Outline each blood parasite and name the species.
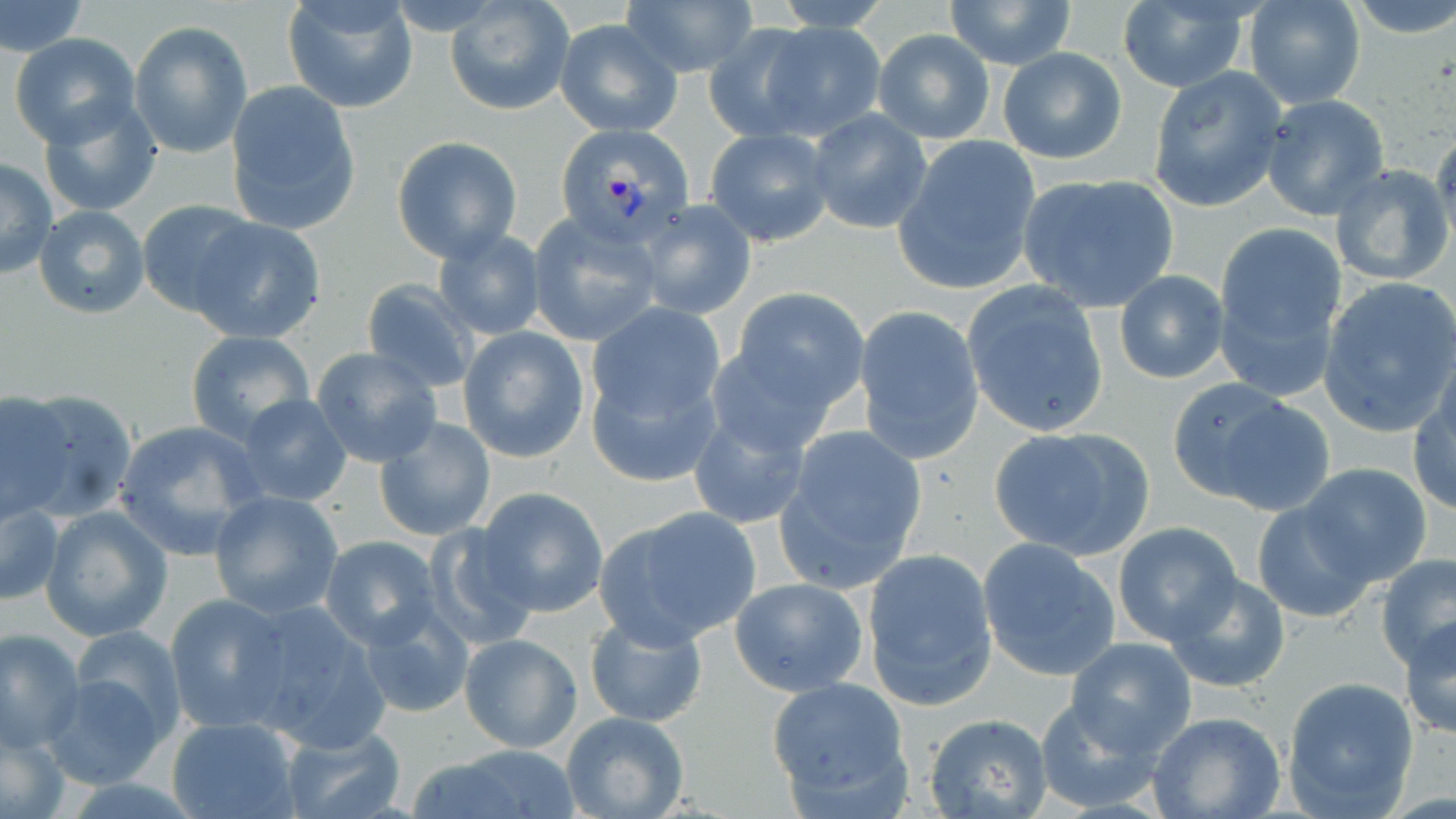

Approximate bounding boxes as named x1/y1/x2/y2 corners in pixels.
Plasmodium vivax-infected red blood cells: (x1=551, y1=127, x2=691, y2=252).
No Plasmodium falciparum, Plasmodium ovale, Plasmodium malariae, Babesia divergens, or Trypanosoma brucei observed.

Uninfected red blood cell locations: (x1=0, y1=0, x2=87, y2=58), (x1=282, y1=0, x2=417, y2=112), (x1=618, y1=0, x2=758, y2=79), (x1=765, y1=0, x2=900, y2=31), (x1=944, y1=0, x2=1076, y2=69), (x1=1243, y1=0, x2=1366, y2=110), (x1=1349, y1=0, x2=1456, y2=40), (x1=445, y1=1, x2=574, y2=115), (x1=1116, y1=1, x2=1252, y2=92), (x1=555, y1=18, x2=682, y2=135), (x1=129, y1=20, x2=252, y2=159), (x1=755, y1=20, x2=888, y2=140), (x1=703, y1=24, x2=823, y2=141), (x1=872, y1=30, x2=996, y2=145), (x1=10, y1=34, x2=141, y2=149), (x1=998, y1=46, x2=1127, y2=165), (x1=1147, y1=66, x2=1288, y2=213), (x1=225, y1=83, x2=360, y2=235), (x1=38, y1=92, x2=165, y2=220), (x1=1260, y1=93, x2=1390, y2=219), (x1=806, y1=109, x2=933, y2=236), (x1=705, y1=128, x2=834, y2=246), (x1=1430, y1=129, x2=1456, y2=252), (x1=392, y1=136, x2=523, y2=263), (x1=893, y1=136, x2=1042, y2=296), (x1=0, y1=159, x2=56, y2=279), (x1=1330, y1=163, x2=1456, y2=285), (x1=1017, y1=173, x2=1180, y2=312), (x1=136, y1=198, x2=260, y2=316), (x1=635, y1=200, x2=757, y2=320), (x1=33, y1=203, x2=150, y2=319), (x1=527, y1=216, x2=661, y2=346), (x1=189, y1=217, x2=327, y2=344), (x1=1213, y1=221, x2=1346, y2=378), (x1=433, y1=229, x2=546, y2=341), (x1=1112, y1=270, x2=1230, y2=384), (x1=1317, y1=276, x2=1456, y2=436), (x1=359, y1=279, x2=478, y2=392), (x1=962, y1=280, x2=1111, y2=438), (x1=730, y1=287, x2=871, y2=411), (x1=588, y1=302, x2=726, y2=429), (x1=854, y1=305, x2=985, y2=461), (x1=458, y1=327, x2=589, y2=462), (x1=185, y1=330, x2=314, y2=444), (x1=705, y1=333, x2=852, y2=454), (x1=310, y1=346, x2=443, y2=468), (x1=586, y1=363, x2=723, y2=490), (x1=1408, y1=375, x2=1456, y2=517), (x1=1166, y1=379, x2=1314, y2=511), (x1=0, y1=392, x2=76, y2=521), (x1=234, y1=394, x2=353, y2=508), (x1=686, y1=407, x2=813, y2=530), (x1=374, y1=416, x2=495, y2=541), (x1=113, y1=418, x2=266, y2=559), (x1=773, y1=424, x2=928, y2=592), (x1=988, y1=425, x2=1155, y2=561), (x1=1298, y1=464, x2=1433, y2=585), (x1=474, y1=487, x2=610, y2=617), (x1=209, y1=491, x2=344, y2=619), (x1=1, y1=498, x2=63, y2=607), (x1=1251, y1=499, x2=1381, y2=624), (x1=38, y1=506, x2=173, y2=642), (x1=596, y1=506, x2=762, y2=648), (x1=425, y1=521, x2=541, y2=647), (x1=1113, y1=523, x2=1242, y2=645), (x1=320, y1=537, x2=442, y2=648), (x1=976, y1=540, x2=1122, y2=682), (x1=862, y1=545, x2=998, y2=712), (x1=1376, y1=555, x2=1456, y2=666), (x1=1166, y1=574, x2=1291, y2=693), (x1=730, y1=577, x2=871, y2=698), (x1=164, y1=594, x2=297, y2=733), (x1=357, y1=600, x2=474, y2=719), (x1=239, y1=601, x2=391, y2=747), (x1=584, y1=610, x2=707, y2=727), (x1=1402, y1=616, x2=1456, y2=742), (x1=0, y1=627, x2=84, y2=753), (x1=67, y1=627, x2=188, y2=751), (x1=458, y1=633, x2=582, y2=752), (x1=1066, y1=636, x2=1197, y2=756), (x1=39, y1=671, x2=171, y2=792), (x1=766, y1=675, x2=913, y2=812), (x1=1281, y1=675, x2=1421, y2=818), (x1=1032, y1=695, x2=1166, y2=812), (x1=562, y1=711, x2=690, y2=819), (x1=1149, y1=712, x2=1286, y2=819), (x1=924, y1=714, x2=1054, y2=819), (x1=167, y1=717, x2=299, y2=819), (x1=1, y1=723, x2=69, y2=819), (x1=278, y1=726, x2=408, y2=819), (x1=412, y1=744, x2=583, y2=818). Slide-level diagnosis: Plasmodium vivax. Light microscopy. Image is 1456×819 pixels. Thin blood film. May-Grünwald-Giemsa-stained preparation. Captured at 1000x magnification. One field of a larger specimen.